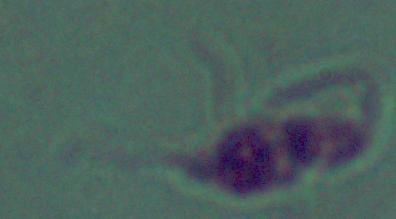

Photomicrograph. 1000x magnification. A Leishmania parasite is seen.